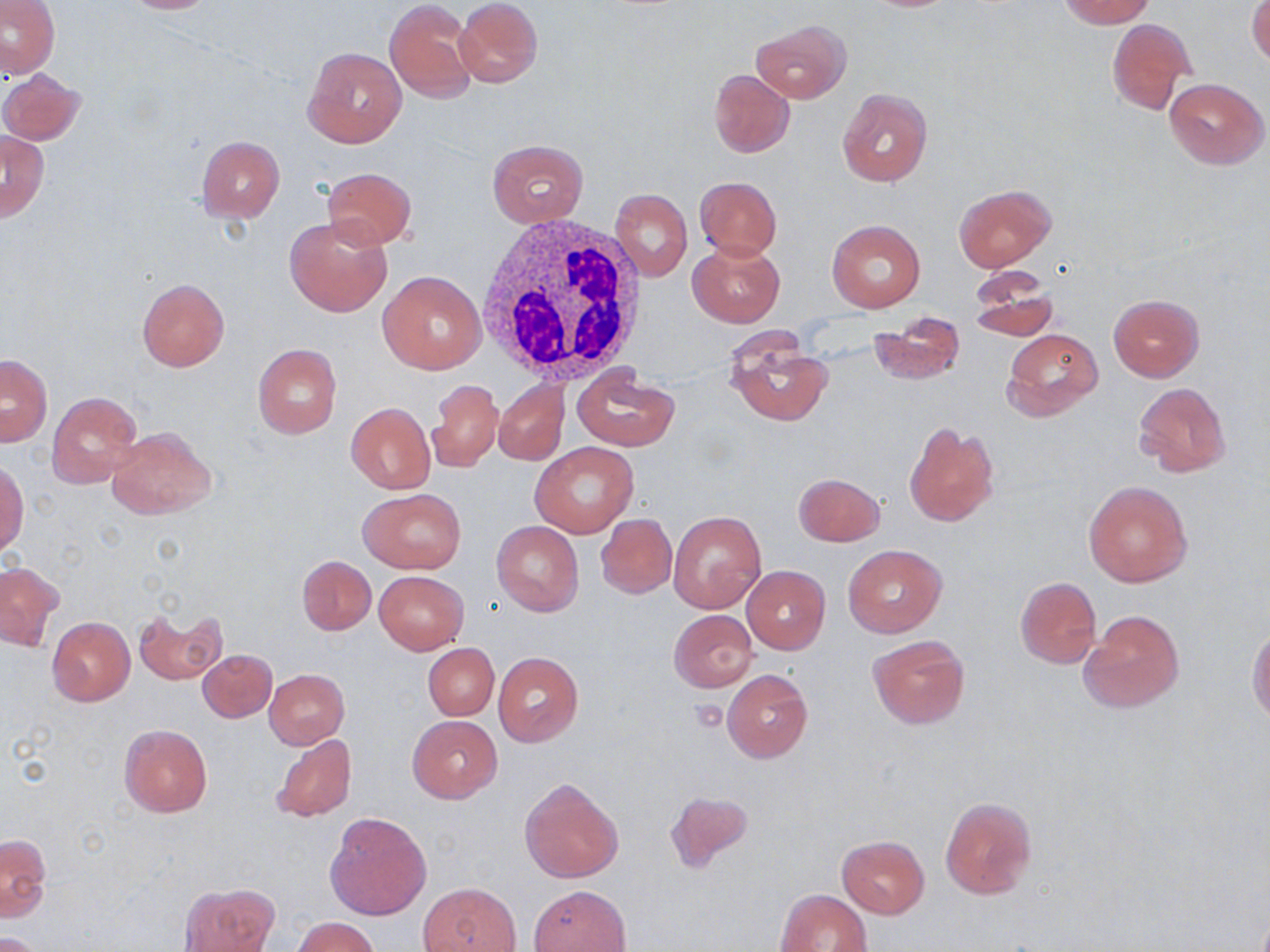

slide_level_diagnosis: negative for blood parasites
uninfected_red_blood_cell_locations: 'approximate bounding boxes as (x1, y1, x2, y2) in pixels: (2, 0, 60, 78), (112, 0, 224, 14), (384, 0, 478, 102), (454, 0, 541, 87), (1055, 0, 1154, 27), (1246, 1, 1270, 66), (1106, 18, 1195, 115), (750, 19, 850, 103), (302, 45, 407, 147), (1, 68, 85, 145), (708, 69, 794, 158), (1164, 78, 1267, 168), (836, 87, 932, 188), (2, 130, 49, 221), (198, 137, 284, 221), (486, 139, 588, 226), (323, 167, 415, 249), (694, 176, 782, 259), (954, 184, 1056, 271), (610, 188, 692, 280), (284, 213, 393, 318), (827, 219, 925, 312), (689, 239, 785, 326), (967, 269, 1057, 342), (379, 270, 487, 374), (137, 278, 229, 371), (1107, 294, 1205, 381), (868, 312, 964, 386), (1001, 329, 1103, 420), (725, 334, 834, 426), (252, 343, 342, 439), (2, 355, 52, 446), (573, 366, 680, 451), (428, 380, 502, 473), (494, 381, 568, 465), (1133, 382, 1232, 477), (46, 392, 144, 490), (346, 402, 435, 493), (902, 422, 999, 528), (105, 426, 217, 521), (530, 441, 638, 538), (0, 462, 28, 558), (794, 472, 884, 546), (1083, 480, 1193, 588), (358, 489, 465, 573), (669, 511, 766, 613), (597, 513, 677, 598), (492, 521, 585, 616), (842, 544, 946, 637), (298, 555, 376, 635), (1, 561, 63, 651), (741, 565, 830, 654), (375, 571, 469, 654), (1016, 577, 1101, 668), (136, 608, 226, 687), (1080, 609, 1185, 713), (669, 610, 758, 691), (47, 617, 135, 706), (1247, 627, 1270, 725), (868, 634, 970, 729), (423, 643, 499, 720), (198, 650, 277, 722), (493, 653, 583, 746), (264, 669, 349, 748), (723, 669, 812, 762), (407, 716, 501, 802), (118, 723, 213, 817), (271, 732, 356, 821), (519, 777, 624, 883), (664, 789, 755, 873), (938, 797, 1039, 900), (324, 810, 431, 921), (2, 833, 51, 922), (836, 835, 930, 918), (419, 882, 520, 951), (181, 883, 277, 951), (529, 884, 629, 952), (774, 888, 872, 952), (294, 917, 378, 952), (1, 932, 45, 952)'
stain: May-Grünwald-Giemsa
preparation: thin blood smear
modality: optical microscopy
field_of_view: one of a larger specimen
magnification: 1000x
white_blood_cell_locations: 'approximate bounding boxes as (x1, y1, x2, y2) in pixels: (471, 212, 648, 386)'
image_size: 1270×952 pixels